Locate every Plasmodium parasite.
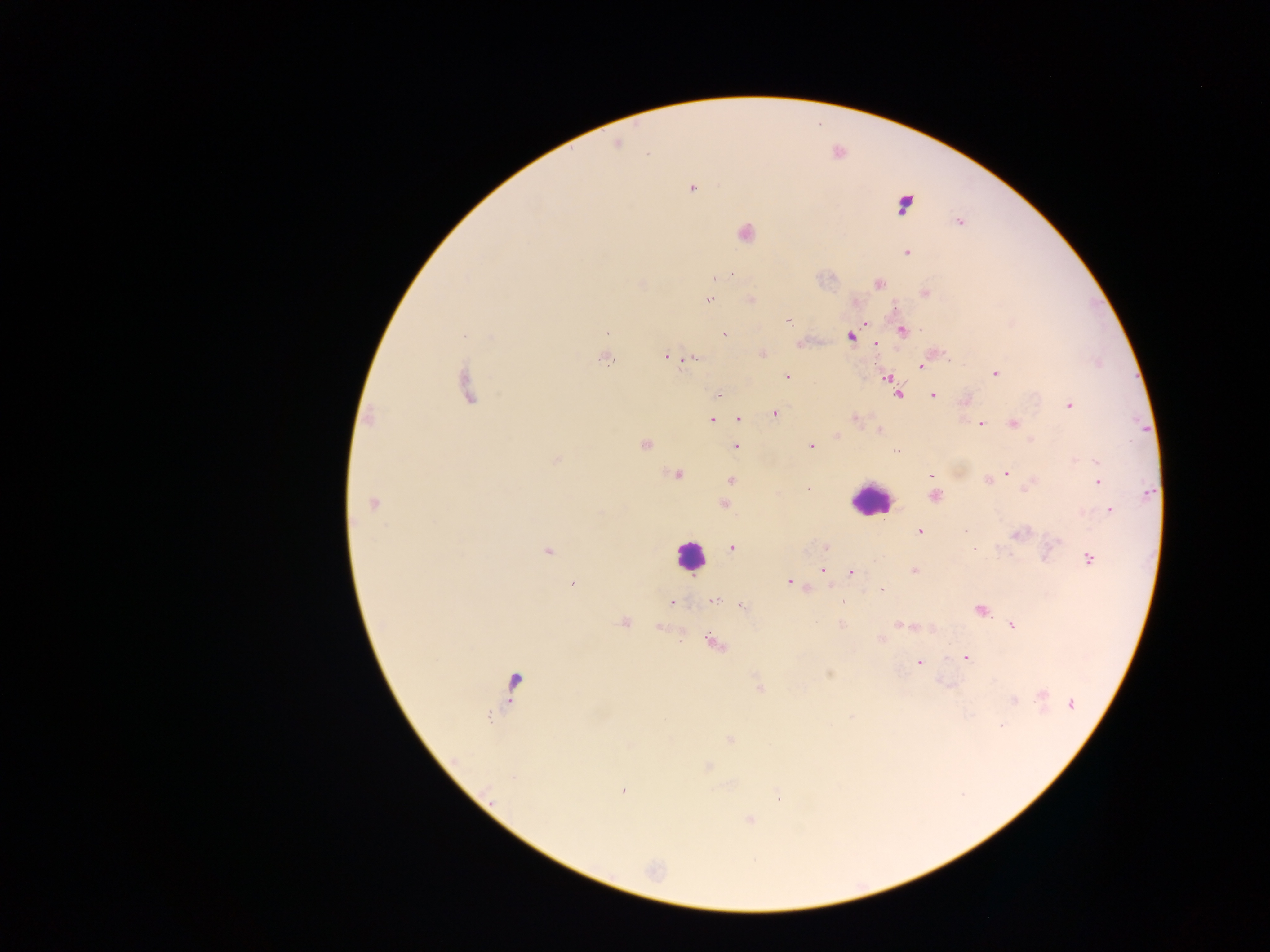
Approximate centers as {x, y} in pixels.
Plasmodium parasites: {617, 144}, {692, 188}, {904, 204}, {959, 222}, {746, 233}, {906, 253}, {716, 279}, {878, 283}, {925, 293}, {751, 299}, {710, 300}, {788, 321}, {865, 324}, {902, 331}, {607, 332}, {464, 334}, {725, 334}, {851, 337}, {876, 343}, {667, 356}, {696, 357}, {605, 360}, {921, 366}, {996, 373}, {787, 377}, {888, 378}, {467, 387}, {898, 393}, {718, 395}, {933, 396}, {965, 401}, {1069, 405}, {775, 414}, {368, 418}, {855, 419}, {711, 420}, {738, 420}, {1013, 423}, {982, 424}, {879, 431}, {837, 436}, {645, 444}, {735, 446}, {810, 446}, {897, 450}, {557, 460}, {1097, 461}, {1006, 473}, {676, 475}, {999, 475}, {930, 477}, {988, 480}, {731, 481}, {1097, 482}, {808, 489}, {935, 495}, {374, 503}, {725, 505}, {1110, 510}, {920, 532}, {1018, 534}, {1057, 541}, {825, 547}, {732, 548}, {974, 548}, {548, 551}, {1090, 559}, {823, 570}, {914, 571}, {851, 572}, {789, 582}, {572, 583}, {882, 590}, {714, 601}, {671, 602}, {842, 602}, {743, 608}, {981, 610}, {624, 621}, {842, 625}, {900, 625}, {1012, 626}, {881, 639}, {714, 644}, {966, 658}, {918, 663}, {829, 674}, {514, 681}, {759, 686}, {1042, 694}, {1013, 700}, {1071, 704}, {852, 716}, {1003, 726}, {731, 739}, {708, 767}, {514, 778}, {623, 791}, {777, 796}, {750, 819}.

Summary:
  - Leukocyte locations: {869, 501}, {689, 556}
  - Image size: 1270×952 pixels
  - Country: Ghana
  - Field of view: single
  - Capture: mobile-phone photograph through a microscope
  - Preparation: thick blood smear